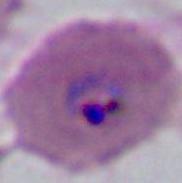
modality = micrograph
identification = Plasmodium
magnification = 400x or 1000x